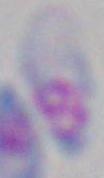
magnification = 1000x
modality = micrograph
identification = Toxoplasma gondii